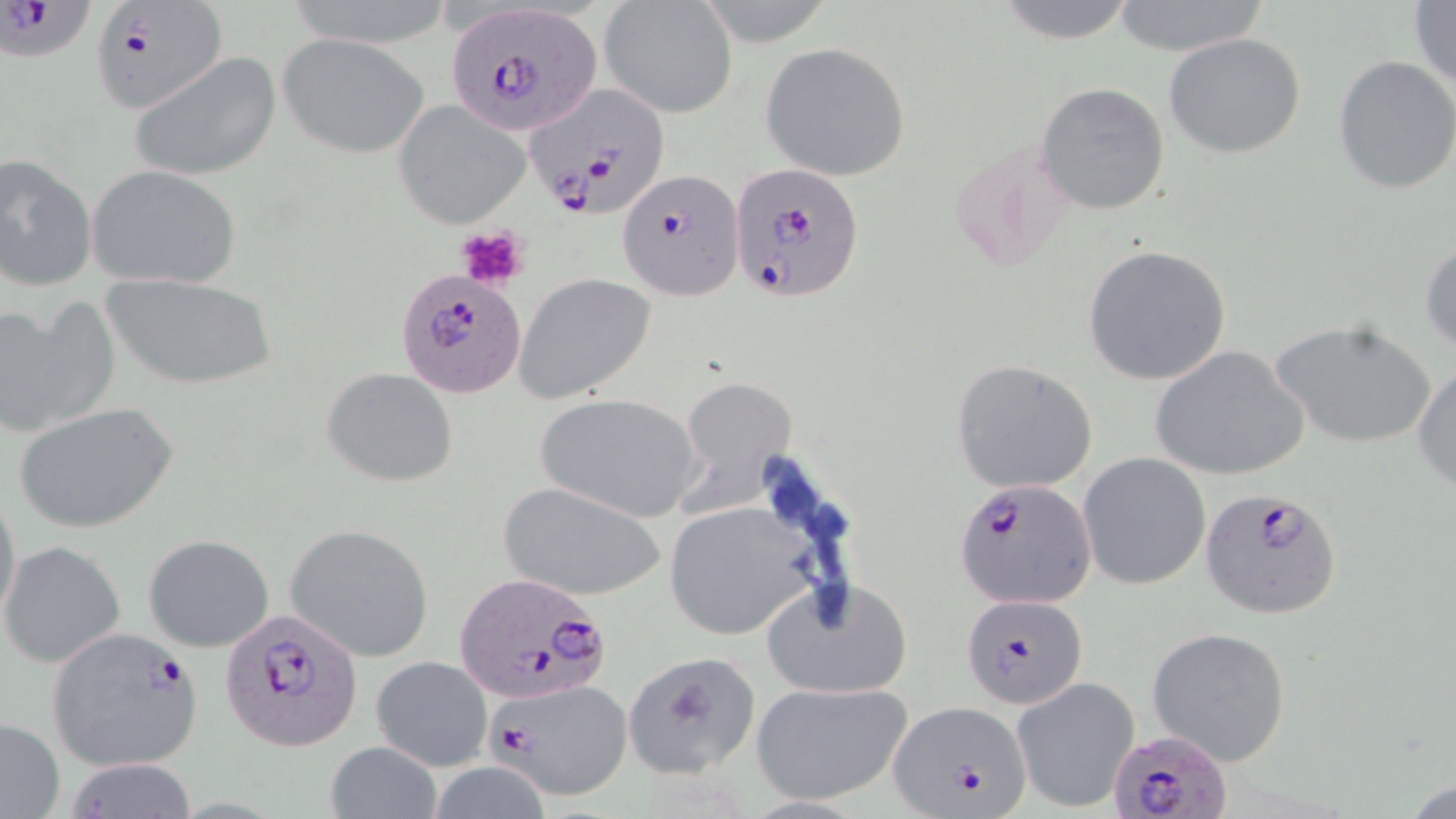 Approximate bounding boxes as (x1,y1)-(x2,y2) corner pairs in pixels. Platelet locations: (454,225)-(530,290). Plasmodium falciparum-infected red blood cell locations: (0,0)-(85,60), (444,1)-(603,138), (94,2)-(228,113), (524,85)-(671,220), (616,168)-(742,300), (728,170)-(861,305), (397,269)-(529,397), (956,478)-(1095,610), (1199,486)-(1343,620), (454,573)-(612,703), (960,594)-(1090,712), (221,605)-(365,754), (44,627)-(204,772), (490,678)-(634,801), (889,701)-(1033,816), (1106,730)-(1233,819). Uninfected red blood cell locations: (284,0)-(459,49), (991,0)-(1141,45), (1408,0)-(1456,94), (1109,1)-(1273,56), (599,2)-(737,120), (279,33)-(429,159), (1164,34)-(1307,160), (760,41)-(913,182), (131,52)-(282,182), (1332,55)-(1456,196), (1036,81)-(1170,216), (394,101)-(529,229), (0,155)-(98,291), (87,165)-(242,289), (1420,240)-(1456,351), (1081,244)-(1231,385), (98,273)-(281,390), (516,274)-(657,401), (0,298)-(119,440), (1271,319)-(1436,450), (1150,345)-(1308,482), (951,359)-(1099,494), (1413,363)-(1456,493), (321,367)-(459,486), (681,375)-(796,482), (535,392)-(704,521), (16,401)-(179,536), (1080,452)-(1210,590), (499,481)-(670,601), (0,485)-(22,636), (661,502)-(819,640), (284,525)-(434,661), (142,534)-(274,653), (1,541)-(127,668), (763,578)-(911,699), (1147,626)-(1292,766), (622,650)-(763,778), (372,655)-(492,771), (1011,677)-(1140,813), (749,680)-(914,806), (0,719)-(66,819), (325,741)-(442,819), (61,758)-(199,818). Slide-level diagnosis: Plasmodium falciparum. Single field of view. Thin blood smear. Optical microscopy. May-Grünwald-Giemsa-stained preparation. Image is 1456×819 pixels. Captured at 1000x magnification.